Give the position of every Plasmodium parasite visible.
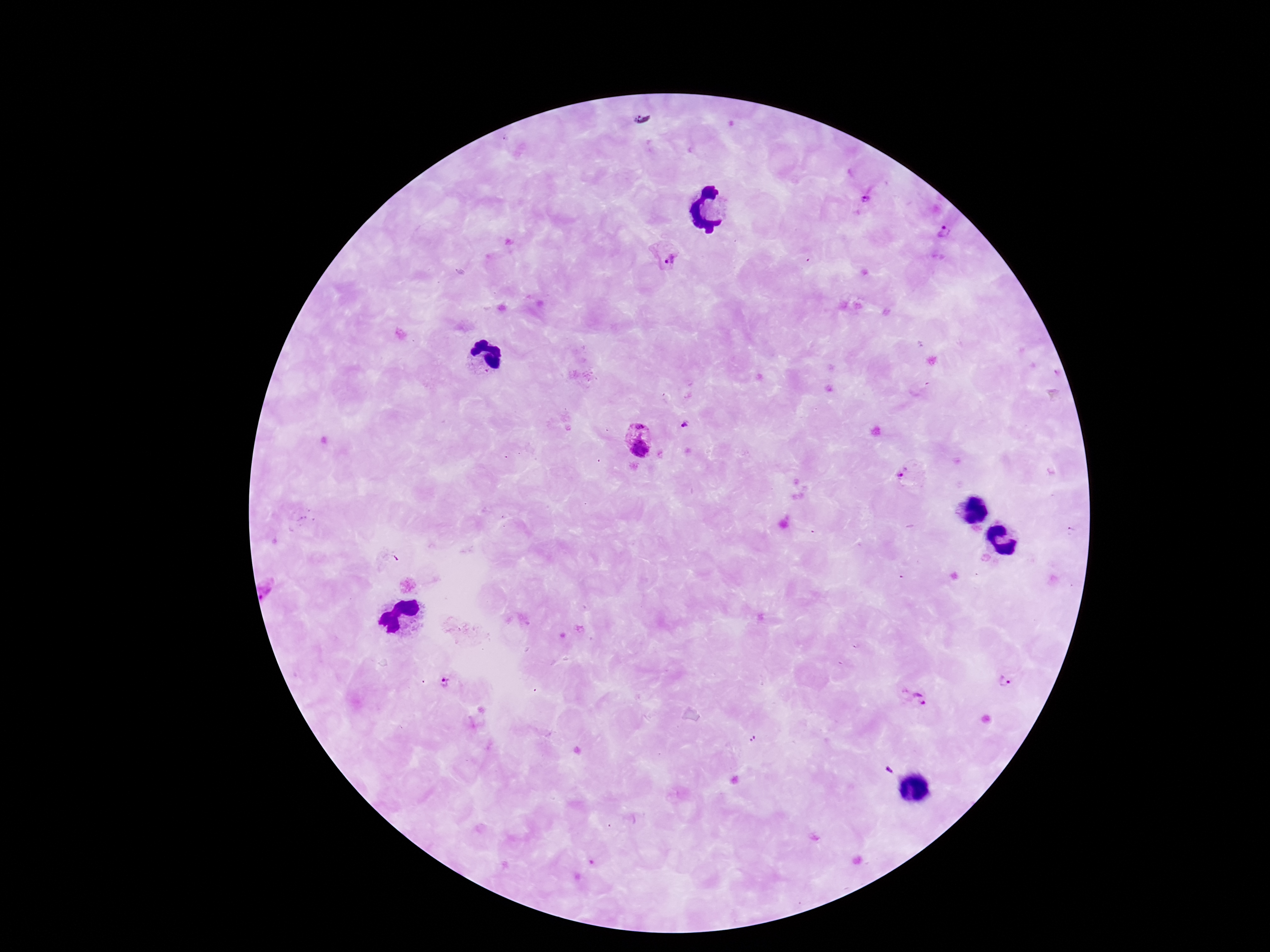

Approximate centers as (x, y) in pixels.
Plasmodium parasites: (865, 198), (947, 232), (667, 257), (685, 425), (639, 438), (909, 474), (1007, 681), (447, 685), (917, 699), (753, 739), (889, 770).

Summary:
  - Magnification: 100x
  - Stain: Giemsa
  - Patient malaria status: infected
  - Image size: 1270×952 pixels
  - Field of view: single
  - Capture: smartphone camera through the microscope eyepiece
  - Preparation: thick blood smear